State which parasite is depicted.
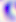
This is Toxoplasma gondii.

Photomicrograph. 400x magnification.